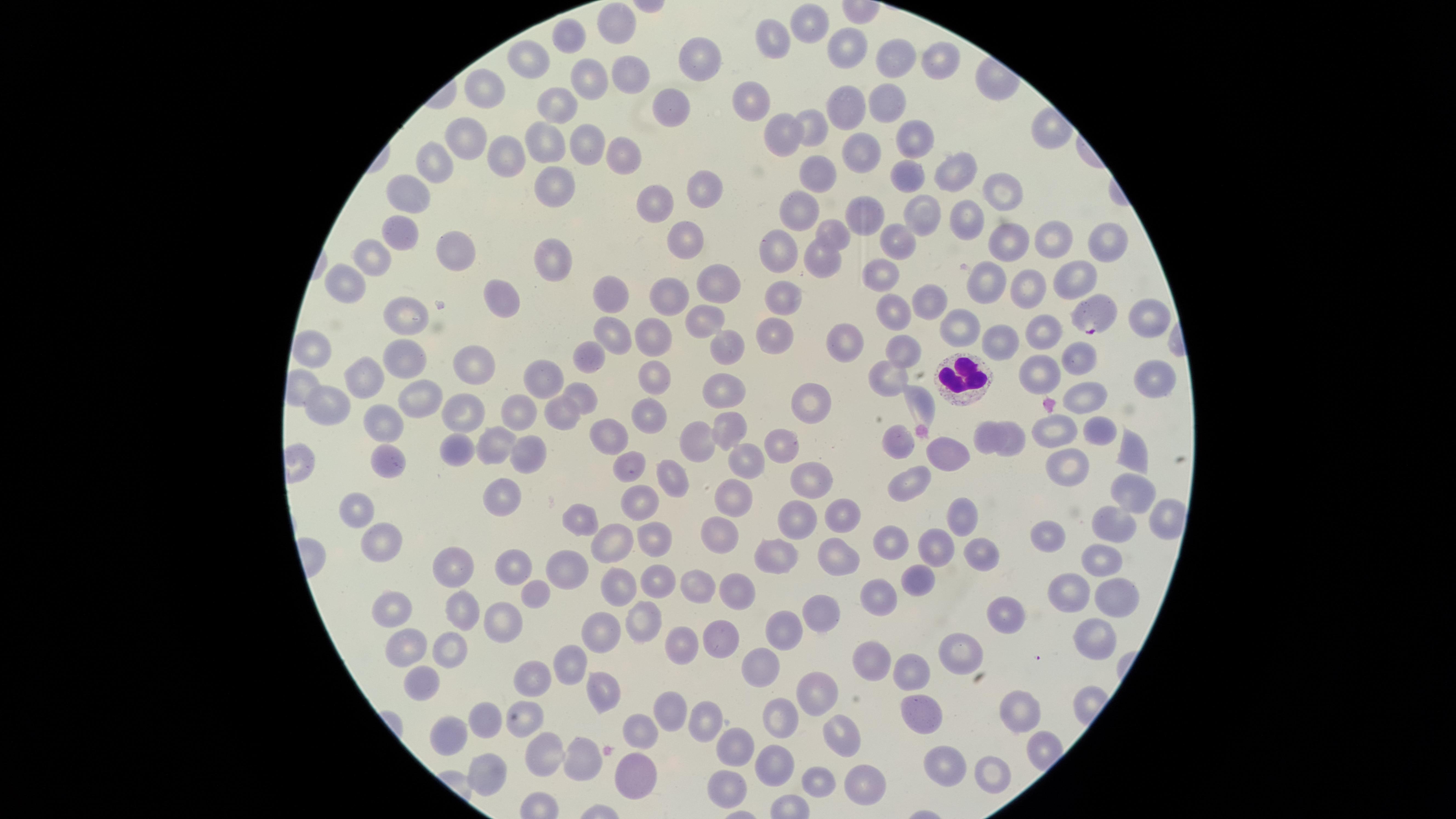 Approximate marker points, in pixels from the top-left corner. White blood cells: (x=961, y=380). Parasitized red blood cells: (x=1094, y=318). Uninfected red blood cells: (x=808, y=22), (x=610, y=24), (x=566, y=37), (x=777, y=40), (x=844, y=47), (x=531, y=58), (x=696, y=58), (x=939, y=58), (x=891, y=59), (x=626, y=73), (x=580, y=83), (x=485, y=90), (x=756, y=97), (x=672, y=100), (x=879, y=103), (x=833, y=108), (x=555, y=109), (x=808, y=128), (x=780, y=134), (x=910, y=136), (x=547, y=139), (x=584, y=141), (x=463, y=142), (x=619, y=148), (x=861, y=152), (x=501, y=156), (x=431, y=168), (x=817, y=171), (x=955, y=173), (x=906, y=177), (x=558, y=183), (x=699, y=187), (x=999, y=189), (x=408, y=195), (x=651, y=204), (x=804, y=207), (x=872, y=210), (x=924, y=216), (x=964, y=220), (x=397, y=226), (x=828, y=233), (x=682, y=237), (x=1049, y=239), (x=1002, y=240), (x=894, y=241), (x=1102, y=242), (x=445, y=247), (x=776, y=247), (x=555, y=250), (x=377, y=255), (x=818, y=258), (x=878, y=266), (x=1074, y=270), (x=988, y=278), (x=719, y=280), (x=344, y=285), (x=1027, y=286), (x=613, y=291), (x=669, y=297), (x=785, y=300), (x=924, y=302), (x=506, y=303), (x=892, y=309), (x=406, y=313), (x=1149, y=316), (x=955, y=323), (x=700, y=324), (x=773, y=329), (x=1045, y=330), (x=609, y=333), (x=648, y=333), (x=997, y=339), (x=312, y=345), (x=731, y=345), (x=840, y=350), (x=903, y=350), (x=588, y=354), (x=407, y=355), (x=1079, y=356), (x=471, y=365), (x=1039, y=367), (x=545, y=370), (x=365, y=374), (x=656, y=376), (x=883, y=376), (x=1147, y=378), (x=579, y=393), (x=722, y=394), (x=1085, y=394), (x=424, y=396), (x=325, y=401), (x=520, y=401), (x=923, y=401), (x=807, y=409), (x=467, y=410), (x=648, y=412), (x=558, y=413), (x=379, y=425), (x=1047, y=426), (x=1095, y=426), (x=724, y=429), (x=984, y=433), (x=602, y=435), (x=696, y=438), (x=1013, y=440), (x=492, y=441), (x=779, y=444), (x=895, y=444), (x=459, y=447), (x=947, y=449), (x=524, y=452), (x=1131, y=456), (x=742, y=459), (x=386, y=465), (x=629, y=465), (x=1069, y=465), (x=804, y=474), (x=909, y=477), (x=673, y=482), (x=733, y=492), (x=508, y=495), (x=1132, y=496), (x=639, y=502), (x=360, y=505), (x=841, y=507), (x=796, y=513), (x=579, y=518), (x=965, y=518), (x=1161, y=520), (x=1110, y=526), (x=715, y=531), (x=1051, y=533), (x=651, y=536), (x=378, y=540), (x=611, y=541), (x=930, y=541), (x=887, y=543), (x=771, y=545), (x=973, y=553), (x=1091, y=556), (x=841, y=557), (x=518, y=559), (x=451, y=563), (x=570, y=568), (x=651, y=577), (x=914, y=580), (x=530, y=587), (x=609, y=587), (x=700, y=587), (x=1064, y=592), (x=744, y=593), (x=875, y=594), (x=1111, y=598), (x=389, y=602), (x=455, y=605), (x=822, y=608), (x=494, y=614), (x=1017, y=617), (x=640, y=618), (x=783, y=627), (x=717, y=631), (x=597, y=632), (x=407, y=640), (x=682, y=640), (x=1089, y=640), (x=455, y=644), (x=960, y=653), (x=758, y=659), (x=864, y=660), (x=567, y=664), (x=911, y=669), (x=416, y=677), (x=533, y=677), (x=815, y=692), (x=598, y=695), (x=924, y=707), (x=1021, y=710), (x=667, y=712), (x=784, y=715), (x=518, y=716), (x=707, y=718), (x=486, y=724), (x=637, y=730), (x=830, y=735), (x=446, y=736), (x=735, y=742), (x=546, y=755), (x=577, y=757), (x=945, y=761), (x=773, y=767), (x=990, y=769), (x=484, y=775), (x=631, y=777), (x=865, y=779), (x=820, y=783), (x=728, y=787). Presence: malaria parasites identified. Smartphone photograph through the microscope eyepiece. The visible region is circular. Single field of view. Image is 1456×819 pixels. Giemsa-stained preparation. Thin smear of blood. Species: Plasmodium falciparum.